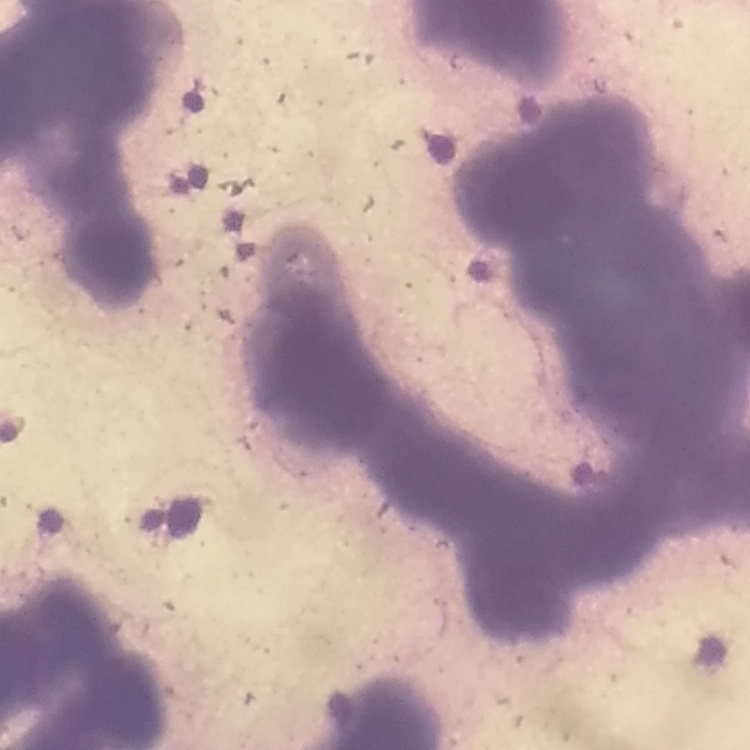

{
  "red_blood_cell_morphology": "rouleaux formation",
  "stain": "Field's or Giemsa",
  "image_type": "one tile cut from a larger photomicrograph",
  "preparation": "thin peripheral smear"
}